Classify this cell by malaria status.
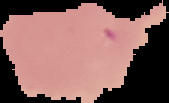
Uninfected.

Image is 169×103 pixels. Segmented cell region on a black background. From a thin blood smear.